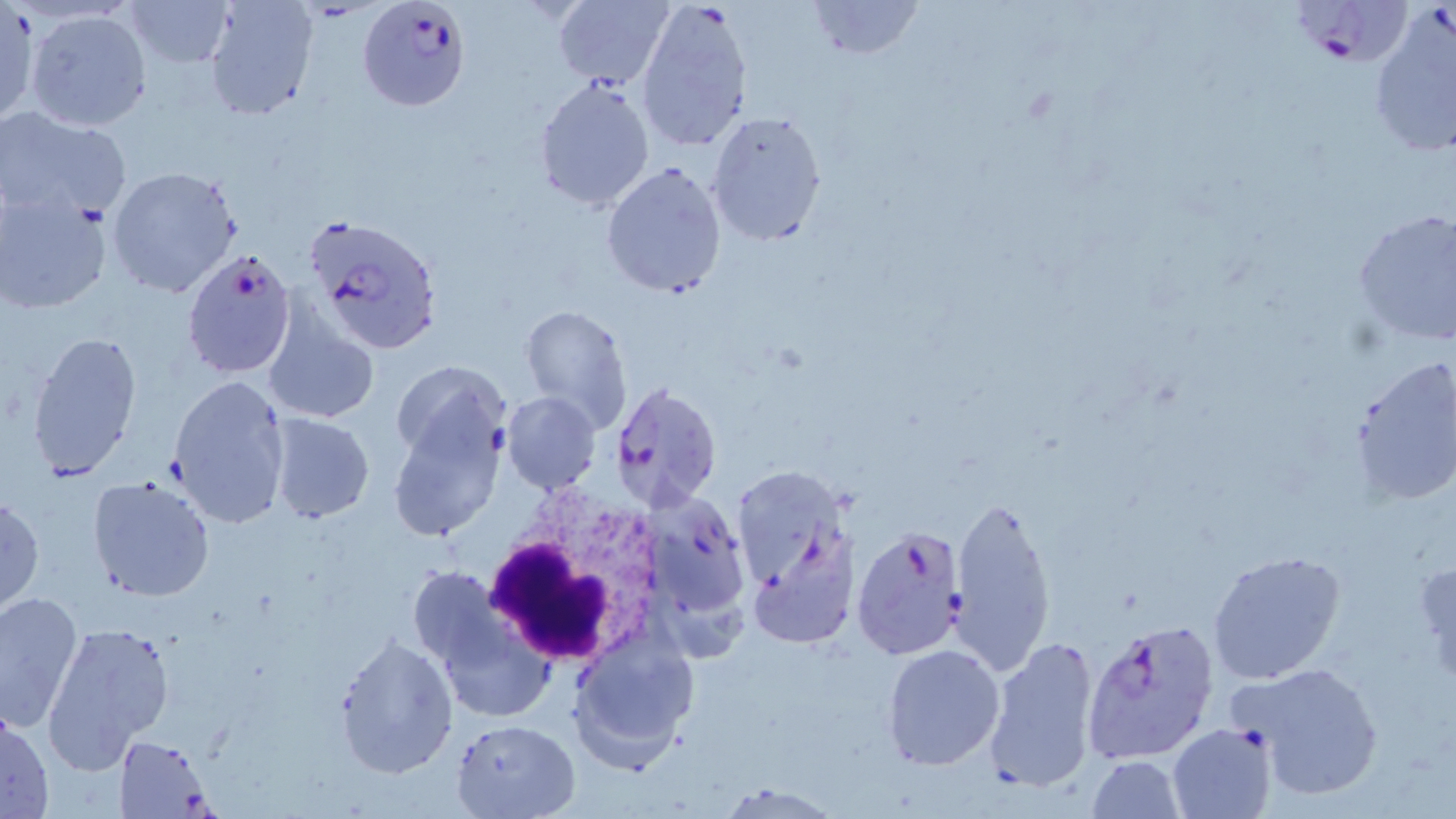

Summary:
  - Coordinate format: approximate bounding boxes as (x1,y1)-(x2,y2) corner pairs in pixels
  - Uninfected red blood cell locations: (120,0)-(238,69), (204,0)-(318,123), (634,0)-(753,155), (801,0)-(925,60), (552,1)-(673,89), (0,4)-(37,127), (25,8)-(151,132), (534,76)-(655,213), (706,108)-(829,247), (0,109)-(133,224), (602,162)-(728,299), (106,166)-(243,299), (0,187)-(115,316), (1351,208)-(1455,345), (260,301)-(379,426), (518,305)-(631,430), (25,328)-(143,481), (1349,356)-(1456,506), (392,362)-(508,544), (168,375)-(290,528), (501,391)-(600,494), (266,414)-(375,524), (88,476)-(215,603), (949,493)-(1056,675), (0,494)-(45,616), (750,538)-(857,647), (1206,550)-(1349,687), (1414,556)-(1456,690), (0,590)-(83,734), (41,620)-(174,773), (570,628)-(699,771), (332,633)-(458,780), (984,634)-(1100,794), (881,643)-(1005,771), (1231,661)-(1388,802), (0,710)-(51,818), (451,717)-(579,817), (1167,723)-(1278,818), (114,734)-(216,816), (1085,754)-(1186,818), (714,780)-(841,817)
  - Plasmodium falciparum-infected red blood cell locations: (358,0)-(472,111), (1286,1)-(1425,70), (1367,5)-(1456,159), (303,212)-(442,354), (181,250)-(296,378), (609,381)-(723,511), (643,497)-(749,620), (850,524)-(968,660), (1081,618)-(1220,765)
  - White blood cell locations: (478,491)-(671,671)
  - Slide-level diagnosis: Plasmodium falciparum
  - Image size: 1456×819 pixels
  - Magnification: 1000x
  - Preparation: thin blood smear
  - Stain: May-Grünwald-Giemsa
  - Field of view: one of a larger specimen
  - Modality: optical microscopy